Assess this cell for malaria.
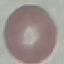
Uninfected.

Summary:
  - Image type: cell patch, automatically extracted from a larger field of view and resized to 64 × 64 pixels
  - Capture: smartphone through the microscope eyepiece
  - Stain: Giemsa
  - Preparation: thin blood film